Find each parasitized red blood cell.
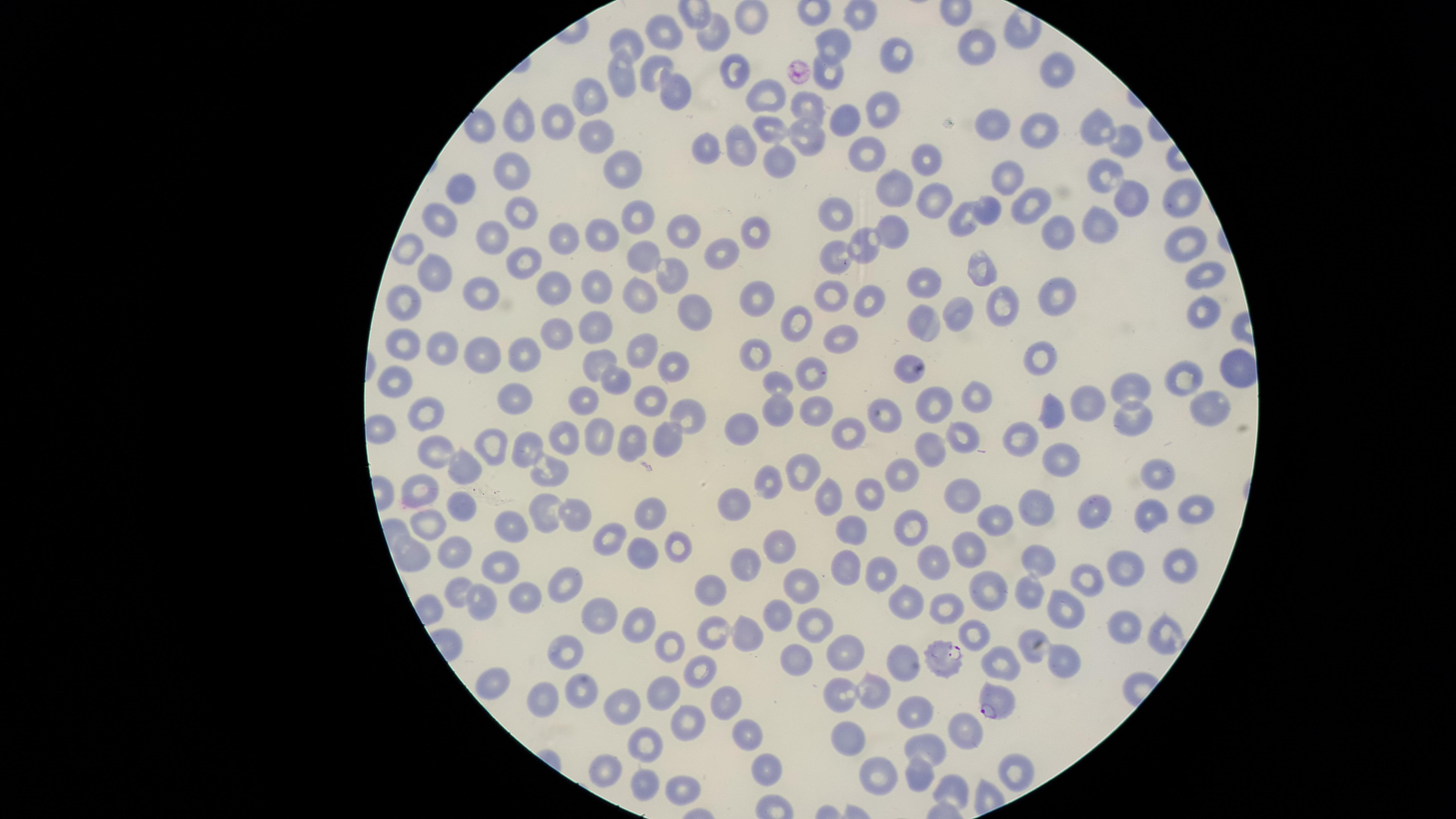
Approximate marker points as [x, y] in pixels.
Parasitized red blood cells: [942, 656], [990, 702].

Approximate marker points as [x, y] in pixels. Uninfected red blood cells: [861, 15], [751, 18], [716, 35], [665, 40], [837, 42], [980, 44], [632, 45], [898, 51], [734, 71], [831, 71], [1057, 72], [654, 74], [625, 76], [677, 90], [770, 98], [593, 99], [807, 107], [879, 108], [843, 118], [523, 119], [562, 119], [993, 122], [1094, 123], [484, 124], [772, 127], [1037, 128], [593, 136], [810, 137], [742, 141], [1129, 142], [867, 148], [707, 150], [780, 160], [926, 162], [621, 165], [515, 172], [1009, 173], [1107, 176], [893, 186], [461, 190], [1181, 196], [1134, 197], [934, 199], [1036, 205], [990, 206], [639, 213], [524, 214], [965, 216], [842, 218], [439, 221], [1100, 222], [894, 226], [687, 231], [1051, 233], [756, 235], [493, 236], [599, 236], [563, 237], [864, 242], [1189, 242], [408, 247], [725, 250], [644, 253], [836, 253], [525, 264], [983, 267], [674, 274], [1208, 275], [432, 276], [925, 282], [550, 286], [597, 289], [475, 290], [832, 290], [642, 291], [755, 295], [1057, 295], [869, 300], [1000, 302], [403, 303], [691, 310], [958, 311], [1203, 311], [922, 318], [796, 327], [595, 332], [555, 333], [842, 335], [407, 344], [439, 345], [646, 348], [520, 352], [760, 353], [484, 354], [1038, 362], [599, 364], [903, 364], [1236, 364], [675, 368], [815, 371], [1187, 373], [393, 381], [781, 381], [619, 382], [1128, 383], [977, 392], [517, 393], [587, 394], [648, 399], [937, 401], [1092, 402], [812, 405], [1051, 410], [1208, 410], [424, 411], [780, 411], [1135, 415], [688, 416], [890, 416], [744, 427], [381, 428], [850, 431], [963, 433], [631, 434], [1019, 435], [562, 436], [598, 436], [668, 439], [497, 444], [439, 449], [528, 449], [928, 451], [1064, 458], [466, 464], [550, 468], [808, 469], [903, 470], [1155, 473], [768, 479], [869, 489], [964, 493], [419, 496], [823, 498], [740, 504], [464, 506], [1033, 506], [1198, 508], [651, 509], [547, 512], [1153, 512], [1090, 515], [576, 517], [984, 518], [512, 522], [914, 525], [429, 527], [852, 529], [611, 534], [782, 542], [966, 544], [675, 547], [457, 549], [640, 550], [416, 553], [1041, 561], [747, 562], [844, 562], [934, 564], [1129, 564], [501, 565], [1179, 566], [883, 573], [1083, 577], [561, 581], [805, 586], [459, 589], [712, 589], [985, 591], [1029, 592], [522, 593], [904, 600], [476, 606], [601, 606], [1067, 609], [942, 610], [780, 615], [1125, 623], [813, 625], [640, 626], [751, 632], [718, 635], [981, 636], [1034, 636], [1160, 636], [674, 643], [569, 650], [852, 651], [796, 658], [1062, 659], [1007, 661], [905, 665], [702, 669], [489, 684], [583, 687], [669, 691], [875, 693], [838, 695], [545, 699], [727, 699], [628, 703], [910, 718], [691, 723], [970, 728], [743, 731], [848, 738], [646, 746], [921, 748], [767, 767], [608, 770], [876, 772], [915, 772], [1010, 772], [677, 786], [643, 789], [957, 791]. Image is 1456×819 pixels. One field of view of the specimen. Photographed with a smartphone camera through the microscope eyepiece. Species: Plasmodium falciparum. Thin blood film. Giemsa stain. The visible region is circular.